Identify the parasite.
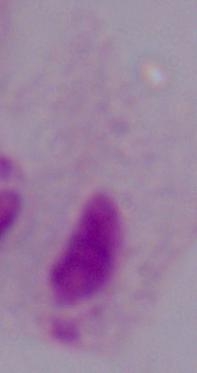

A trichomonad.

Summary:
  - Magnification: 1000x
  - Modality: micrograph